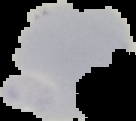

Result: negative for Plasmodium parasites. Segmented cell region on a black background. From a thin blood film. Image is 136×121 pixels.